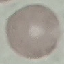 Result: no malaria parasites detected. Giemsa-stained preparation. Acquired by smartphone through the microscope eyepiece. Cell patch, automatically extracted from a larger field of view and resized to 64 × 64 pixels. Thin smear of blood.